Identify the parasite.
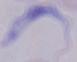
This is a trypanosome.

Captured at 1000x magnification. Photomicrograph.